Outline each uninfected red blood cell.
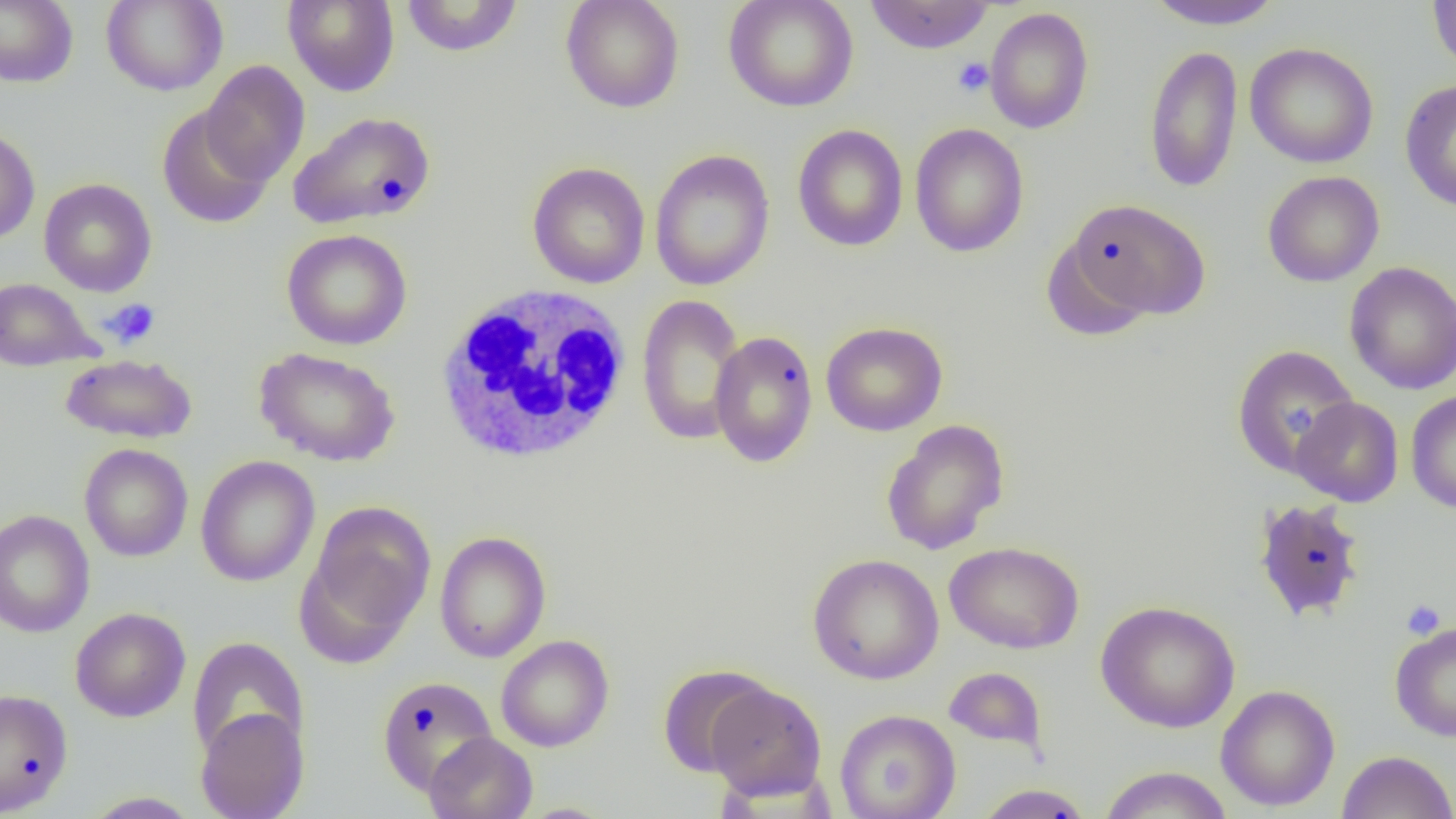

Approximate bounding boxes as (x1, y1, x2, y2) in pixels.
Uninfected red blood cells: (0, 0, 78, 87), (101, 0, 228, 96), (400, 0, 524, 57), (560, 0, 685, 113), (723, 0, 859, 112), (864, 0, 994, 54), (1146, 0, 1286, 30), (1427, 0, 1456, 75), (283, 1, 400, 97), (984, 7, 1094, 134), (1245, 42, 1379, 168), (1143, 44, 1243, 193), (200, 60, 310, 186), (1399, 80, 1456, 212), (157, 105, 274, 230), (288, 110, 437, 230), (909, 123, 1029, 257), (792, 124, 909, 252), (0, 125, 40, 244), (649, 149, 775, 292), (526, 161, 651, 288), (1262, 171, 1384, 287), (39, 178, 157, 297), (1066, 197, 1211, 321), (282, 228, 412, 350), (1041, 237, 1154, 344), (1344, 261, 1456, 395), (0, 278, 99, 371), (636, 294, 746, 445), (821, 321, 948, 436), (708, 330, 819, 468), (1231, 344, 1360, 480), (254, 346, 401, 467), (60, 353, 198, 444), (1405, 390, 1456, 513), (1290, 397, 1404, 507), (881, 419, 1010, 556), (79, 443, 193, 562), (195, 456, 320, 587), (1252, 498, 1367, 623), (301, 500, 436, 654), (0, 509, 95, 637), (434, 531, 551, 663), (944, 541, 1084, 654), (807, 553, 944, 684), (1096, 600, 1240, 733), (70, 607, 191, 722), (1389, 621, 1456, 742), (496, 634, 614, 752), (186, 637, 310, 762), (657, 664, 774, 778), (943, 666, 1048, 756), (376, 675, 498, 795), (705, 680, 827, 800), (1215, 685, 1340, 811), (0, 687, 74, 815), (195, 707, 309, 819), (834, 709, 961, 819), (424, 732, 538, 819), (1337, 750, 1456, 819), (1098, 765, 1232, 818), (974, 783, 1094, 819), (81, 792, 201, 818).

Summary:
  - Platelet locations: (953, 57, 993, 97), (100, 298, 161, 350), (1286, 403, 1314, 435), (1401, 598, 1446, 640)
  - White blood cell locations: (434, 283, 635, 465)
  - Slide-level diagnosis: negative for blood parasites
  - Modality: light microscopy
  - Field of view: one of a larger specimen
  - Preparation: thin blood smear
  - Magnification: 1000x
  - Image size: 1456×819 pixels